Classify this cell by malaria status.
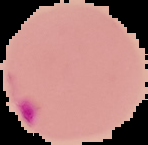
Parasitized.

image_size: 148×145 pixels
preparation: thin blood smear
image_type: cell region segmented out of the field of view; surrounding area masked to black